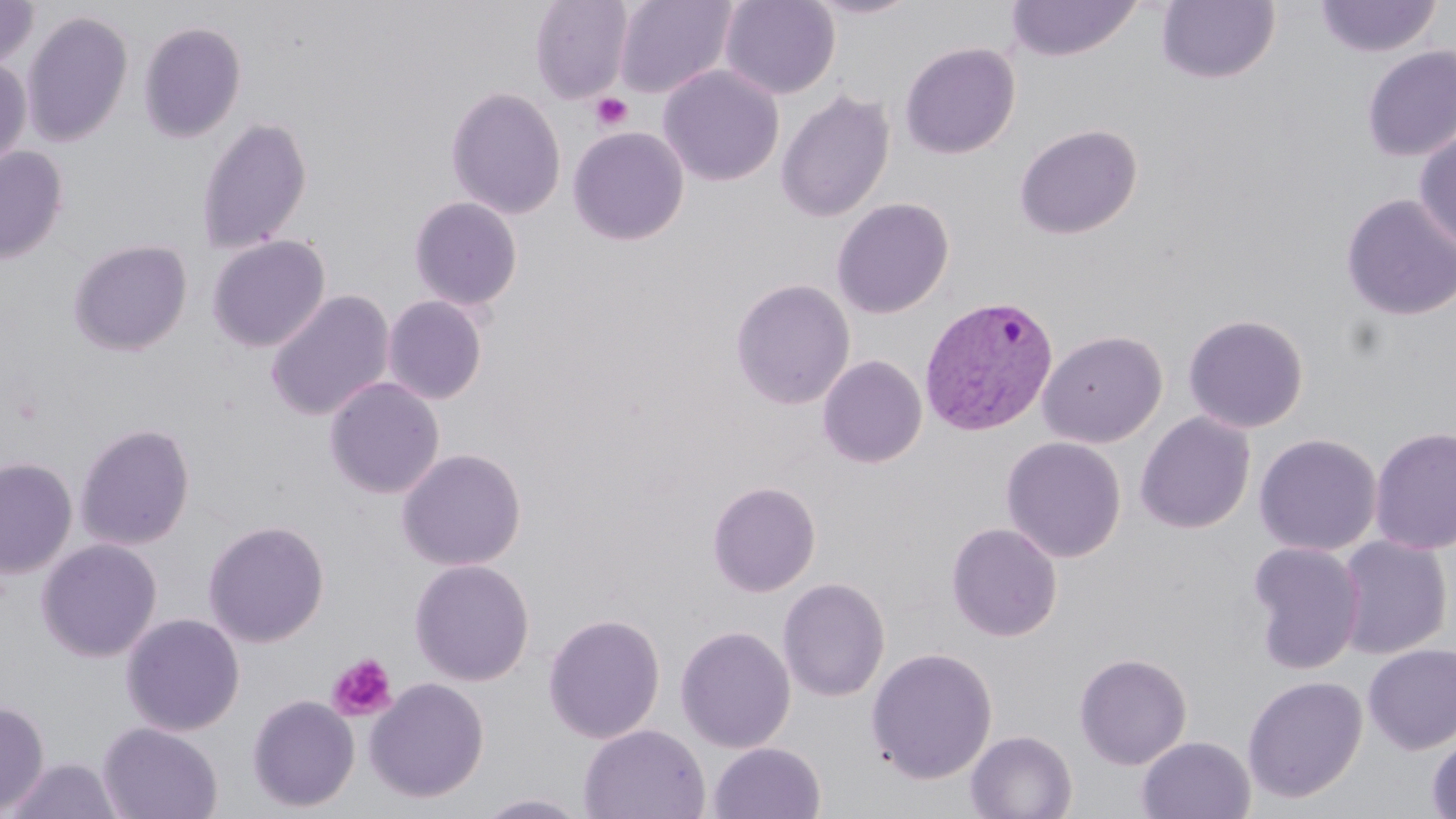

Summary:
  - Coordinate format: approximate bounding boxes as (x1,y1)-(x2,y2) corner pairs in pixels
  - Uninfected red blood cell locations: (529,0)-(633,103), (613,0)-(738,99), (720,0)-(840,99), (803,0)-(922,19), (1314,0)-(1442,58), (0,1)-(38,70), (1005,1)-(1141,62), (1157,1)-(1279,84), (21,10)-(133,147), (138,21)-(247,143), (900,42)-(1020,159), (1361,46)-(1456,162), (0,56)-(31,168), (658,65)-(784,187), (445,86)-(566,219), (775,89)-(894,223), (196,116)-(312,255), (1013,124)-(1142,239), (568,126)-(689,245), (1413,128)-(1456,253), (0,146)-(68,264), (1340,193)-(1456,322), (409,195)-(523,312), (831,197)-(955,319), (207,235)-(331,352), (68,238)-(193,356), (731,278)-(855,409), (265,290)-(395,422), (383,295)-(488,404), (1183,314)-(1309,433), (1038,329)-(1168,448), (817,355)-(927,468), (323,377)-(445,499), (1135,412)-(1255,534), (73,422)-(196,550), (1369,425)-(1456,556), (1254,433)-(1382,556), (1001,436)-(1126,563), (396,447)-(527,572), (0,457)-(77,578), (707,481)-(821,597), (202,518)-(330,648), (946,522)-(1063,642), (1336,535)-(1452,659), (36,538)-(163,663), (1246,542)-(1365,674), (409,559)-(535,686), (778,577)-(890,702), (121,612)-(245,736), (543,613)-(666,744), (675,625)-(796,753), (1363,644)-(1456,755), (865,647)-(998,783), (1074,652)-(1192,770), (1242,675)-(1367,803), (365,677)-(490,803), (247,694)-(360,812), (0,699)-(49,816), (97,722)-(223,819), (579,724)-(710,819), (966,730)-(1077,819), (1426,732)-(1456,819), (1136,735)-(1255,819), (708,742)-(826,819), (4,758)-(123,818), (474,793)-(593,818)
  - Platelet locations: (591,93)-(633,131), (328,653)-(398,722)
  - Plasmodium vivax-infected red blood cell locations: (919,295)-(1059,436)
  - Slide-level diagnosis: Plasmodium vivax
  - Image size: 1456×819 pixels
  - Preparation: thin blood film
  - Magnification: 1000x
  - Stain: May-Grünwald-Giemsa
  - Modality: optical microscopy
  - Field of view: one of a larger specimen